Assess this cell for malaria.
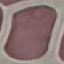
It is uninfected.

Photographed with a smartphone camera at the microscope eyepiece. Giemsa-stained preparation. Thin smear of blood. Cell patch, automatically extracted from a larger field of view and resized to 64 × 64 pixels.